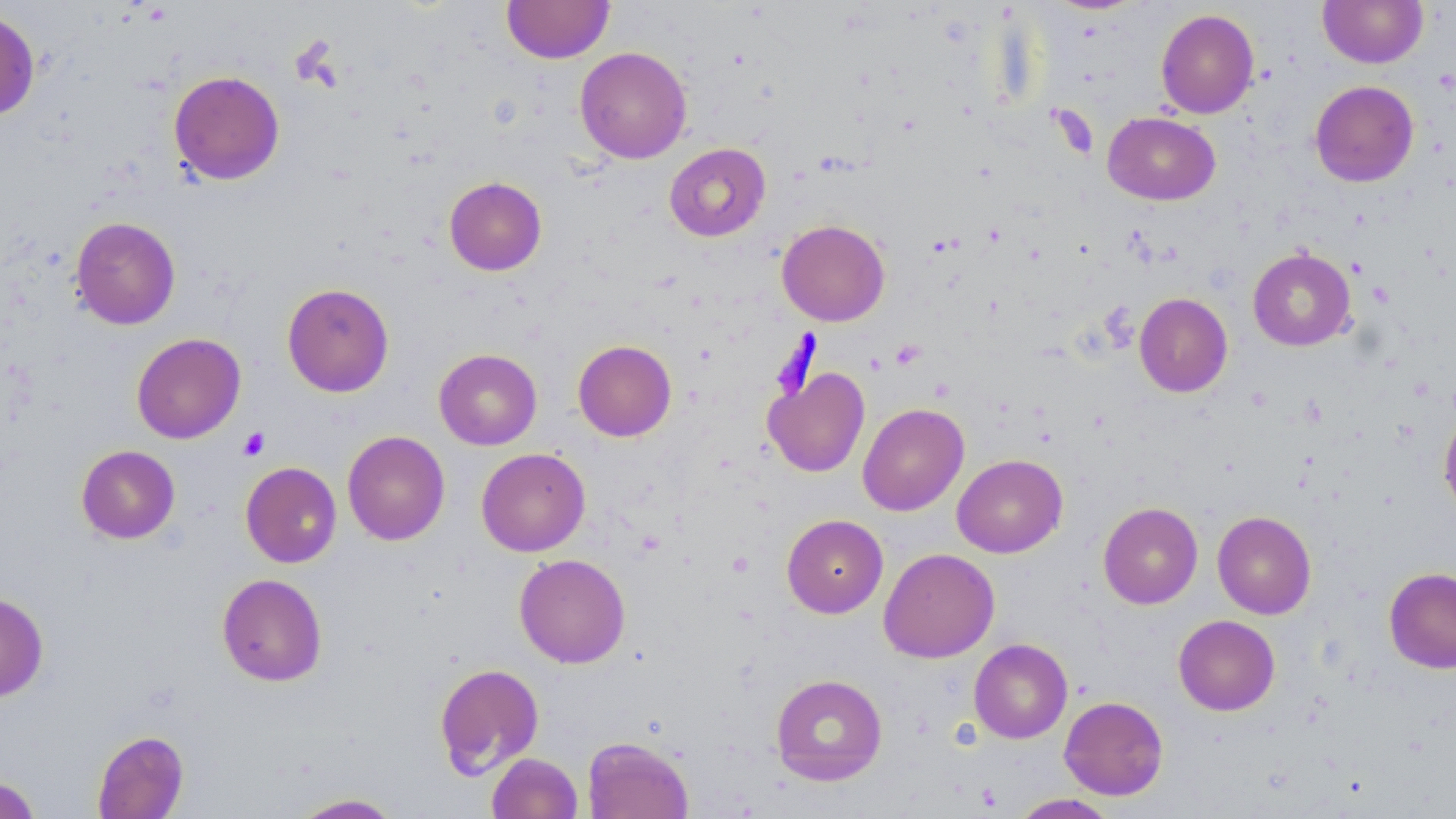

Summary:
  - Coordinate format: approximate bounding boxes as (x1, y1, x2, y2) in pixels
  - Uninfected red blood cell locations: (502, 0, 614, 63), (1318, 0, 1427, 68), (0, 7, 40, 123), (1155, 9, 1259, 119), (575, 46, 691, 163), (169, 70, 285, 185), (1310, 80, 1419, 186), (1103, 112, 1220, 205), (664, 143, 771, 242), (444, 176, 547, 276), (70, 216, 180, 330), (777, 219, 890, 326), (1248, 248, 1356, 351), (281, 282, 394, 397), (1134, 292, 1233, 397), (131, 332, 246, 443), (572, 339, 676, 442), (434, 348, 542, 450), (764, 367, 870, 477), (857, 402, 969, 516), (1438, 409, 1456, 517), (343, 430, 449, 545), (76, 445, 180, 543), (476, 448, 590, 556), (952, 454, 1068, 558), (241, 461, 341, 567), (1098, 502, 1203, 609), (1212, 511, 1316, 619), (782, 514, 888, 618), (879, 548, 999, 663), (514, 553, 630, 668), (1384, 567, 1456, 673), (216, 573, 328, 686), (0, 591, 49, 701), (1173, 614, 1280, 716), (969, 638, 1072, 743), (434, 663, 545, 779), (770, 673, 888, 786), (1059, 696, 1168, 800), (92, 729, 189, 819), (582, 737, 694, 818), (486, 752, 583, 818), (0, 776, 41, 818), (289, 792, 404, 818), (1010, 793, 1118, 818)
  - Platelet locations: (1349, 258, 1368, 278), (1367, 281, 1395, 305), (891, 339, 925, 369), (238, 428, 270, 460), (726, 551, 755, 577)
  - Slide-level diagnosis: no evidence of blood parasites
  - Modality: light microscopy
  - Image size: 1456×819 pixels
  - Field of view: single
  - Stain: May-Grünwald-Giemsa
  - Preparation: thin blood smear
  - Magnification: 1000x